Report the malaria status of this cell.
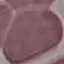
Uninfected.

Acquired by smartphone through the microscope eyepiece. Automatically extracted cell patch, resized to 64 × 64 pixels. Giemsa-stained preparation. Thin smear of blood.